Report the malaria status of this cell.
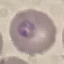
It is parasitized.

Thin blood film. Photographed with a smartphone camera at the microscope eyepiece. Giemsa-stained preparation. Cell patch, automatically extracted from a larger field of view and resized to 64 × 64 pixels.